Locate every Plasmodium ovale-infected red blood cell.
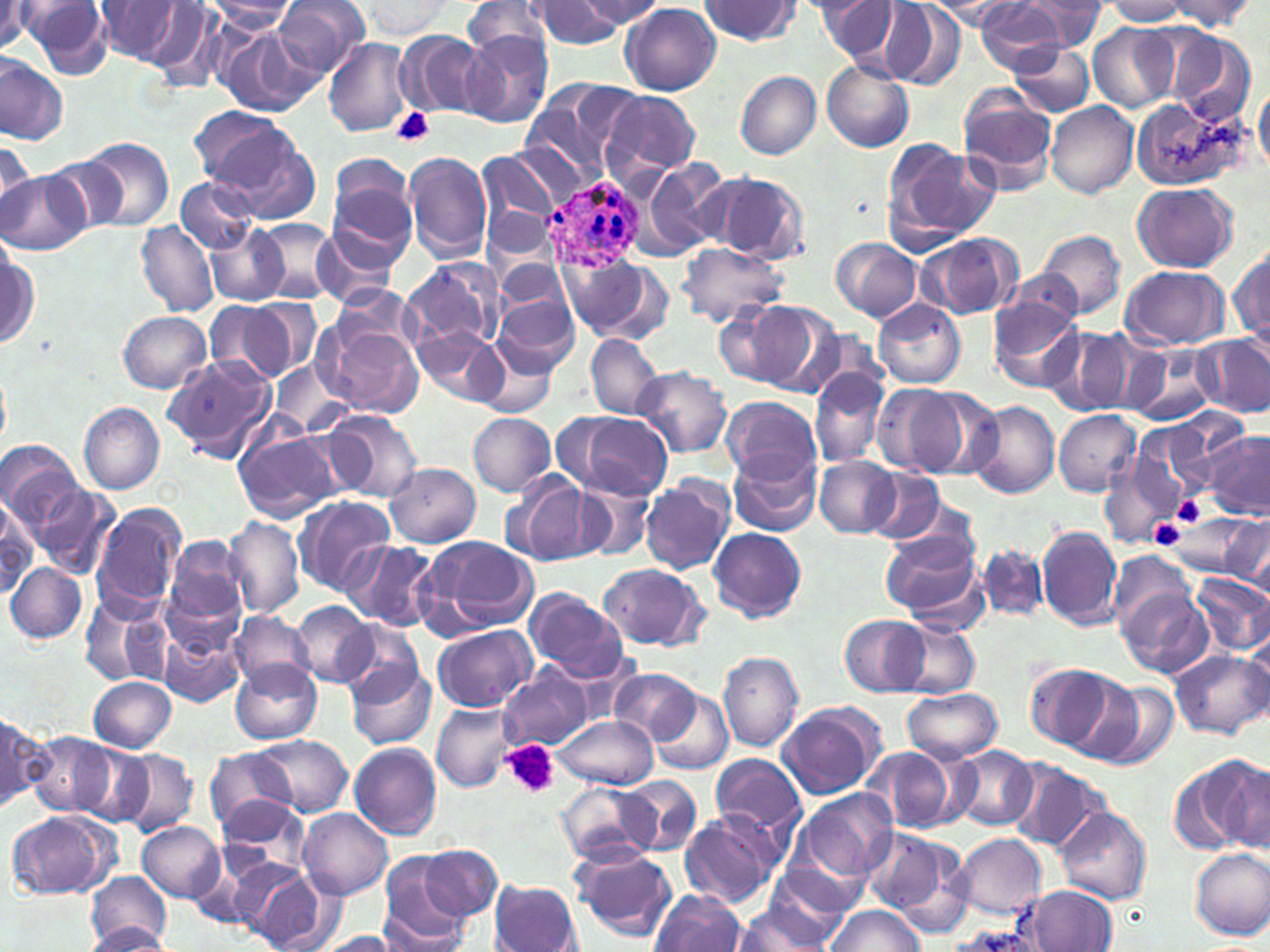

Approximate bounding boxes as (x1,y1)-(x2,y2) corner pairs in pixels.
Plasmodium ovale-infected red blood cells: (543,168)-(647,272).

Summary:
  - Uninfected red blood cell locations: (95,0)-(189,65), (273,0)-(372,79), (358,0)-(454,37), (464,0)-(556,63), (578,0)-(666,28), (698,0)-(799,45), (818,0)-(905,65), (926,0)-(1022,31), (974,0)-(1069,73), (1022,0)-(1109,48), (1105,0)-(1189,27), (535,1)-(622,49), (1166,1)-(1257,31), (20,2)-(115,79), (204,2)-(297,32), (880,2)-(966,92), (0,3)-(34,54), (143,3)-(229,92), (621,4)-(721,95), (1088,24)-(1177,114), (213,25)-(319,118), (398,31)-(487,116), (462,31)-(554,129), (1171,32)-(1259,126), (324,37)-(413,136), (1009,42)-(1095,117), (0,56)-(68,145), (821,59)-(915,152), (736,70)-(820,159), (1254,82)-(1270,177), (520,83)-(636,188), (958,92)-(1055,196), (604,93)-(700,178), (1130,96)-(1243,190), (1045,101)-(1138,199), (188,105)-(296,191), (213,127)-(321,226), (79,137)-(175,232), (884,140)-(999,245), (0,141)-(37,220), (405,151)-(494,262), (326,152)-(411,236), (477,152)-(560,246), (34,156)-(127,237), (636,158)-(733,260), (1,171)-(87,254), (712,174)-(810,265), (176,176)-(256,252), (329,179)-(416,272), (1132,183)-(1237,273), (253,219)-(337,302), (137,221)-(219,316), (208,224)-(288,306), (313,227)-(402,312), (1038,230)-(1126,322), (919,232)-(1022,319), (831,237)-(923,321), (676,241)-(788,328), (1231,243)-(1270,348), (1,244)-(40,350), (403,257)-(504,352), (495,259)-(573,322), (557,259)-(665,341), (1121,265)-(1228,350), (1001,272)-(1084,340), (494,292)-(577,376), (244,297)-(322,378), (873,299)-(965,388), (721,300)-(815,390), (988,300)-(1084,391), (204,302)-(286,380), (118,311)-(212,393), (316,319)-(424,418), (413,325)-(510,407), (1041,328)-(1134,418), (1193,334)-(1270,416), (585,335)-(663,419), (473,340)-(557,417), (1124,349)-(1215,426), (161,355)-(278,460), (268,361)-(352,437), (632,366)-(733,457), (0,369)-(10,450), (808,369)-(890,469), (870,383)-(969,478), (910,385)-(1005,480), (721,395)-(820,483), (967,399)-(1060,499), (79,403)-(165,495), (321,409)-(424,502), (1053,410)-(1141,496), (567,411)-(673,498), (468,413)-(556,496), (232,425)-(342,523), (1202,431)-(1268,516), (1,439)-(84,532), (728,448)-(821,537), (1101,449)-(1184,548), (813,457)-(901,537), (386,463)-(481,546), (861,468)-(948,545), (500,471)-(598,567), (572,477)-(659,563), (639,477)-(734,575), (36,483)-(118,578), (291,494)-(397,596), (0,496)-(40,594), (92,503)-(186,616), (1160,507)-(1266,581), (1220,514)-(1270,590), (224,515)-(306,620), (1036,525)-(1122,629), (709,527)-(807,623), (880,527)-(980,617), (426,536)-(540,631), (167,537)-(247,623), (343,540)-(443,632), (979,544)-(1049,623), (1108,549)-(1194,634), (6,563)-(86,642), (598,563)-(708,651), (1189,573)-(1270,658), (1120,586)-(1213,678), (523,587)-(629,681), (81,595)-(174,690), (290,600)-(377,687), (229,611)-(315,691), (840,614)-(928,697), (891,617)-(981,697), (336,620)-(424,700), (158,623)-(245,708), (432,625)-(536,713), (718,650)-(804,753), (1170,650)-(1269,739), (346,660)-(436,751), (231,661)-(323,744), (1024,661)-(1128,754), (501,665)-(594,750), (610,668)-(701,744), (88,677)-(177,753), (1089,679)-(1180,771), (901,686)-(1003,763), (653,690)-(735,775), (776,700)-(887,799), (432,702)-(516,792), (1,714)-(46,815), (554,714)-(658,790), (28,732)-(114,815), (254,736)-(353,815), (74,743)-(154,826), (348,744)-(442,839), (951,745)-(1037,832), (205,747)-(296,832), (860,747)-(964,833), (118,750)-(198,836), (710,755)-(807,840), (1195,755)-(1270,852), (1006,759)-(1110,853), (621,776)-(702,853), (556,782)-(658,867), (792,788)-(898,887), (218,796)-(310,873), (1055,807)-(1152,905), (299,809)-(392,900), (6,810)-(120,899), (677,810)-(786,909), (136,820)-(226,903), (861,826)-(969,930), (953,832)-(1047,919), (570,844)-(677,941), (420,846)-(502,920), (1189,847)-(1270,941), (379,852)-(470,949), (244,865)-(325,951), (760,868)-(859,946), (85,874)-(172,948), (490,880)-(582,952), (1027,885)-(1117,950), (650,890)-(746,952), (732,903)-(835,950), (822,905)-(925,952), (87,923)-(171,950), (316,931)-(400,951)
  - Platelet locations: (392,108)-(436,147), (1171,494)-(1208,526), (1149,517)-(1185,549), (504,740)-(558,798)
  - Slide-level diagnosis: Plasmodium ovale
  - Magnification: 1000x
  - Modality: optical microscopy
  - Stain: May-Grünwald-Giemsa
  - Preparation: thin blood smear
  - Image size: 1270×952 pixels
  - Field of view: single